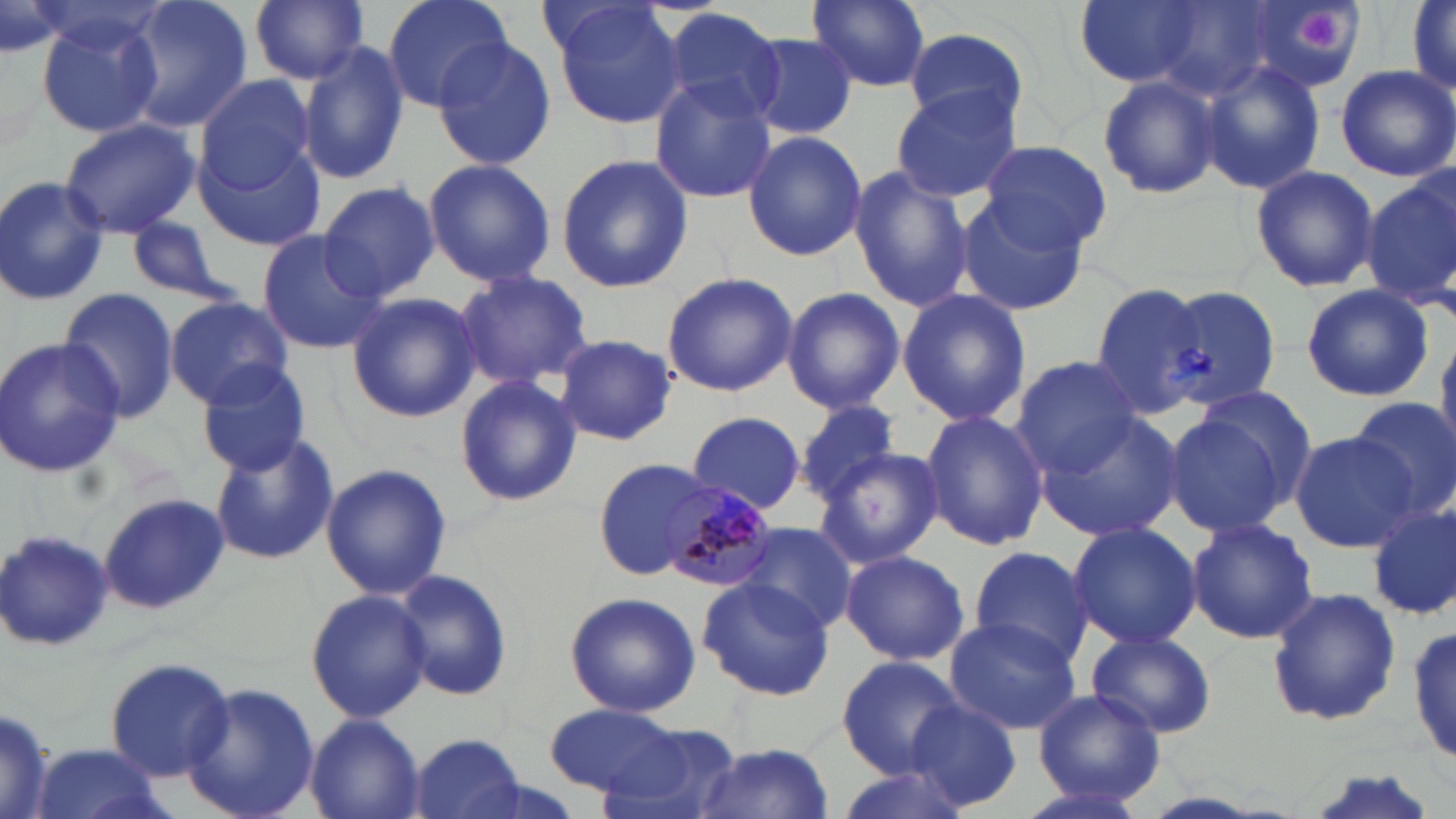 Approximate bounding boxes as [x1, y1, x2, y2] in pixels. Plasmodium malariae-infected red blood cell locations: [662, 483, 783, 594]. Platelet locations: [1293, 6, 1349, 59]. Uninfected red blood cell locations: [116, 0, 255, 133], [250, 0, 370, 84], [381, 0, 515, 111], [807, 0, 931, 91], [1074, 0, 1213, 88], [1246, 0, 1365, 94], [1403, 1, 1456, 100], [548, 2, 688, 130], [1407, 3, 1456, 96], [659, 6, 786, 125], [33, 9, 163, 138], [903, 32, 1028, 129], [745, 34, 859, 139], [430, 38, 557, 170], [297, 40, 409, 185], [1200, 61, 1326, 193], [1334, 64, 1456, 180], [1098, 70, 1221, 201], [194, 74, 320, 198], [647, 80, 776, 205], [889, 85, 1023, 204], [60, 118, 199, 238], [742, 131, 866, 260], [976, 139, 1111, 249], [195, 142, 326, 252], [555, 155, 694, 292], [422, 158, 556, 285], [847, 165, 974, 314], [1248, 165, 1379, 293], [1361, 173, 1456, 312], [0, 175, 110, 305], [318, 180, 440, 302], [955, 197, 1090, 317], [125, 218, 236, 306], [255, 230, 384, 354], [453, 269, 592, 390], [661, 273, 799, 396], [1165, 282, 1283, 414], [1088, 284, 1210, 416], [1302, 285, 1433, 400], [59, 287, 181, 424], [782, 287, 905, 413], [897, 288, 1030, 427], [345, 292, 481, 423], [164, 297, 294, 406], [551, 334, 678, 446], [0, 335, 124, 478], [1436, 335, 1456, 454], [1011, 357, 1144, 474], [197, 364, 316, 476], [453, 375, 582, 506], [1349, 398, 1456, 517], [795, 399, 903, 502], [1161, 407, 1299, 537], [919, 409, 1049, 551], [690, 412, 808, 515], [1036, 412, 1181, 541], [210, 431, 339, 566], [1288, 431, 1417, 552], [815, 447, 943, 569], [593, 458, 719, 576], [321, 462, 451, 601], [97, 494, 229, 615], [1365, 503, 1456, 622], [1185, 518, 1318, 644], [734, 522, 854, 636], [1065, 522, 1203, 648], [0, 526, 116, 653], [968, 546, 1097, 668], [839, 548, 970, 666], [394, 569, 515, 702], [698, 578, 834, 700], [1267, 587, 1404, 726], [305, 588, 432, 723], [564, 591, 700, 718], [944, 615, 1082, 734], [1409, 622, 1456, 767], [1088, 630, 1216, 738], [1055, 637, 1201, 798], [836, 655, 963, 776], [104, 657, 234, 780], [180, 681, 319, 819], [1030, 689, 1167, 807], [906, 701, 1024, 811], [0, 704, 55, 819], [543, 704, 690, 800], [304, 714, 425, 819], [599, 724, 743, 819], [409, 733, 528, 819], [693, 742, 837, 818], [23, 744, 174, 819], [829, 762, 970, 819], [1289, 769, 1445, 819], [1009, 777, 1155, 819]. Slide-level diagnosis: Plasmodium malariae. One field of a larger specimen. May-Grünwald-Giemsa stain. Captured at 1000x magnification. Optical microscopy. Thin blood smear. Image is 1456×819 pixels.